Outline each Plasmodium ovale-infected red blood cell.
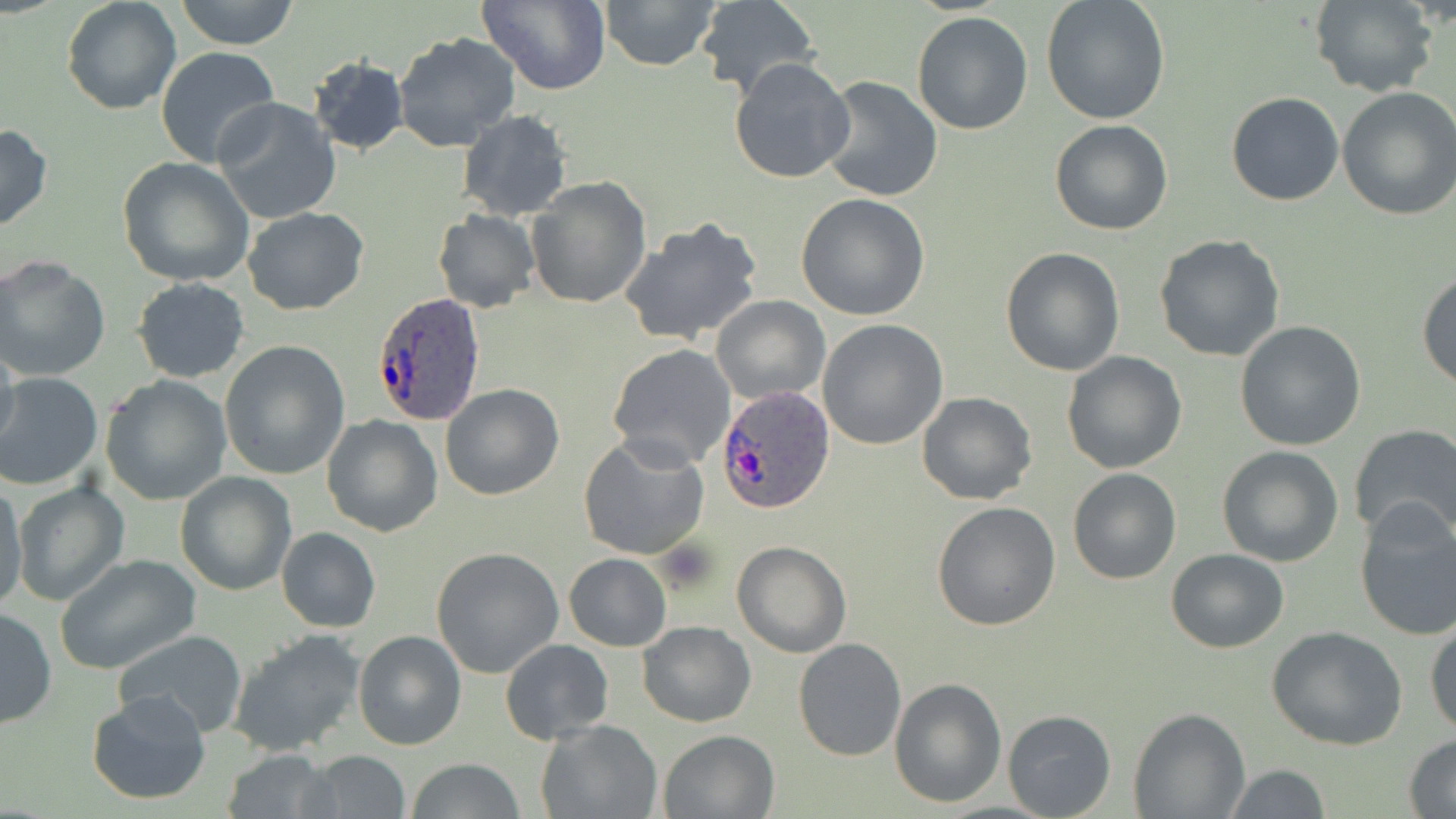
Approximate bounding boxes as (x1,y1)-(x2,y2) corner pairs in pixels.
Plasmodium ovale-infected red blood cells: (371,290)-(487,425), (717,387)-(833,512).

Uninfected red blood cell locations: (62,0)-(181,115), (175,0)-(298,49), (476,0)-(611,93), (599,0)-(721,72), (1310,0)-(1438,98), (694,1)-(819,99), (1040,1)-(1169,123), (912,11)-(1033,135), (392,32)-(522,154), (155,46)-(281,171), (308,55)-(408,156), (729,56)-(856,185), (820,77)-(944,203), (1335,86)-(1456,221), (1226,91)-(1343,205), (212,98)-(342,225), (457,110)-(572,222), (1050,120)-(1175,236), (0,123)-(53,235), (117,156)-(256,287), (527,176)-(650,307), (796,193)-(931,321), (242,207)-(369,315), (433,211)-(540,312), (619,216)-(764,349), (1153,234)-(1286,361), (1000,247)-(1125,376), (0,255)-(111,382), (1417,268)-(1456,390), (132,277)-(250,382), (711,294)-(829,404), (817,319)-(948,449), (1234,321)-(1366,450), (0,333)-(21,457), (219,340)-(350,480), (607,343)-(737,469), (1061,351)-(1187,474), (0,372)-(104,491), (101,374)-(233,504), (439,383)-(564,500), (917,392)-(1037,506), (321,414)-(444,537), (1349,424)-(1456,543), (578,434)-(710,561), (1216,446)-(1345,567), (1067,467)-(1181,584), (176,472)-(295,596), (11,481)-(128,605), (1,482)-(29,607), (932,500)-(1060,631), (1354,502)-(1456,642), (276,527)-(381,632), (732,540)-(851,658), (1165,547)-(1289,653), (431,548)-(564,678), (563,553)-(672,651), (54,554)-(201,675), (0,609)-(56,729), (1425,615)-(1456,738), (637,620)-(756,727), (1267,626)-(1406,750), (114,628)-(246,737), (228,629)-(370,758), (353,630)-(466,750), (501,638)-(613,743), (793,638)-(906,761), (889,675)-(1006,807), (85,691)-(212,806), (1129,708)-(1250,818), (1002,709)-(1117,818), (537,718)-(662,818), (659,729)-(779,818), (1404,734)-(1456,818), (222,748)-(335,819), (302,751)-(411,818), (405,758)-(527,818), (1222,765)-(1332,819). Slide-level diagnosis: Plasmodium ovale. One field of a larger specimen. 1000x magnification. May-Grünwald-Giemsa-stained preparation. Optical microscopy. Image is 1456×819 pixels. Thin blood film.